Assess the morphology of the red blood cells.
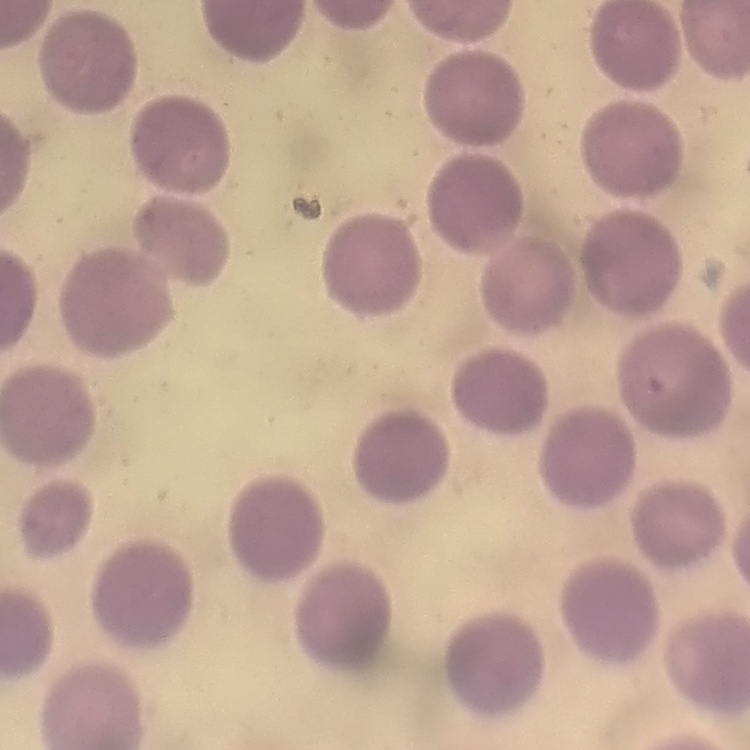
They show no rouleaux formation.

Summary:
  - Preparation: thin blood smear
  - Image type: square crop of a larger photomicrograph
  - Stain: Field's or Giemsa